Assess the morphology of the red blood cells.
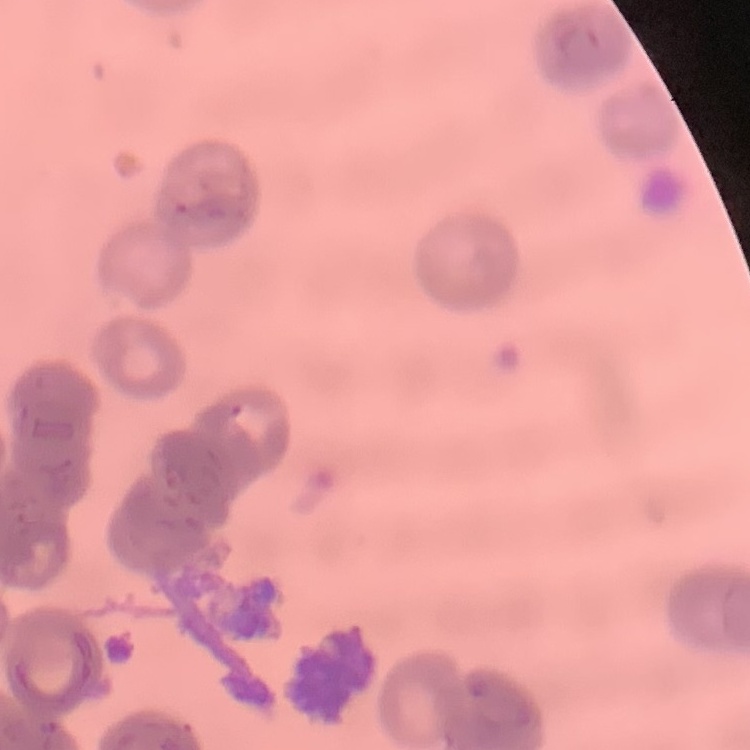
They show rouleaux formation.

Summary:
  - Stain: Field's or Giemsa
  - Preparation: thin peripheral smear
  - Image type: square crop of a larger photomicrograph